Assess this cell for malaria.
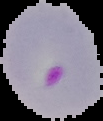
Parasitized.

Summary:
  - Preparation: thin blood film
  - Image size: 103×121 pixels
  - Image type: segmented cell region on a black background